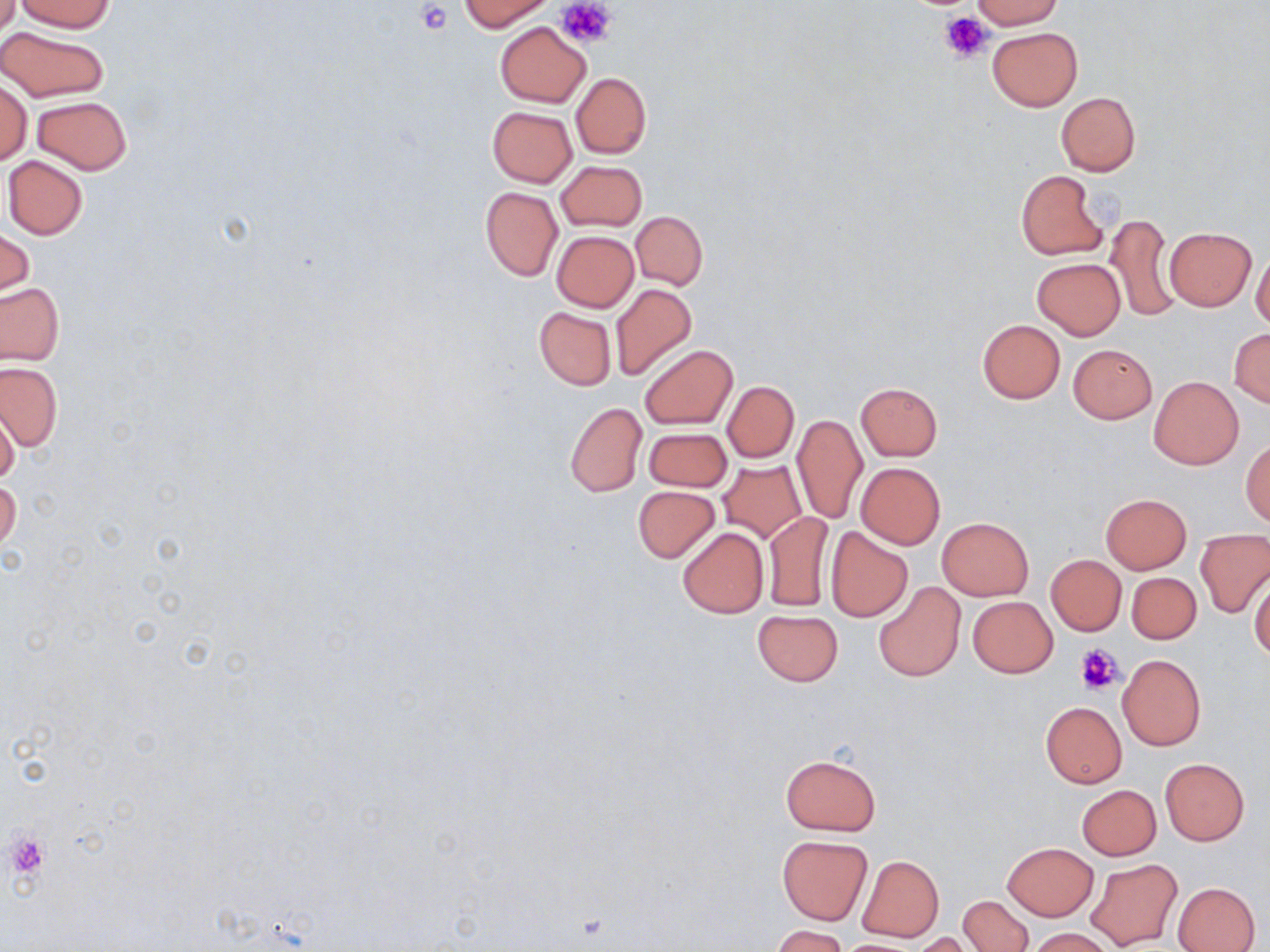 Approximate bounding boxes as (x1,y1)-(x2,y2) corner pairs in pixels. Uninfected red blood cell locations: (0,0)-(21,37), (459,0)-(549,31), (972,0)-(1062,30), (16,1)-(114,32), (496,21)-(590,107), (0,26)-(108,103), (987,26)-(1082,110), (571,72)-(651,158), (1,79)-(32,165), (1056,92)-(1140,175), (33,96)-(131,174), (487,106)-(578,187), (3,156)-(87,240), (556,159)-(646,231), (1015,170)-(1107,261), (480,187)-(562,280), (631,211)-(707,289), (1107,213)-(1180,323), (1165,226)-(1256,310), (1,228)-(34,301), (551,231)-(639,311), (1251,251)-(1270,331), (1033,259)-(1125,339), (0,282)-(65,366), (610,284)-(696,381), (535,308)-(615,389), (977,319)-(1065,404), (1229,329)-(1270,407), (640,344)-(737,429), (1068,344)-(1156,423), (0,362)-(61,452), (1150,376)-(1243,469), (722,381)-(799,463), (856,382)-(942,460), (565,401)-(646,496), (0,409)-(19,487), (793,414)-(867,524), (643,426)-(731,492), (1241,438)-(1269,527), (717,461)-(806,542), (856,463)-(945,548), (1,478)-(21,554), (632,485)-(720,563), (1101,493)-(1192,573), (764,511)-(833,612), (937,517)-(1033,600), (825,527)-(913,621), (677,528)-(769,618), (1196,530)-(1270,617), (1046,555)-(1126,635), (1126,571)-(1201,644), (1249,573)-(1270,662), (872,581)-(965,682), (968,596)-(1058,677), (752,609)-(842,687), (1118,654)-(1205,750), (1040,702)-(1126,788), (780,753)-(881,835), (1160,758)-(1249,845), (1076,784)-(1160,860), (776,834)-(873,925), (1003,842)-(1097,920), (855,854)-(944,943), (1086,858)-(1184,950), (1173,882)-(1260,952), (959,894)-(1033,952), (773,926)-(848,952), (1025,928)-(1116,952), (914,933)-(978,952), (830,938)-(927,951). Platelet locations: (558,0)-(616,49), (415,2)-(454,36), (940,11)-(993,64), (1075,643)-(1125,694), (3,828)-(51,884). Slide-level diagnosis: negative for blood parasites. May-Grünwald-Giemsa-stained preparation. Captured at 1000x magnification. Light microscopy. Image is 1270×952 pixels. One field of a larger specimen. Thin blood film.